Outline each blood parasite and name the species.
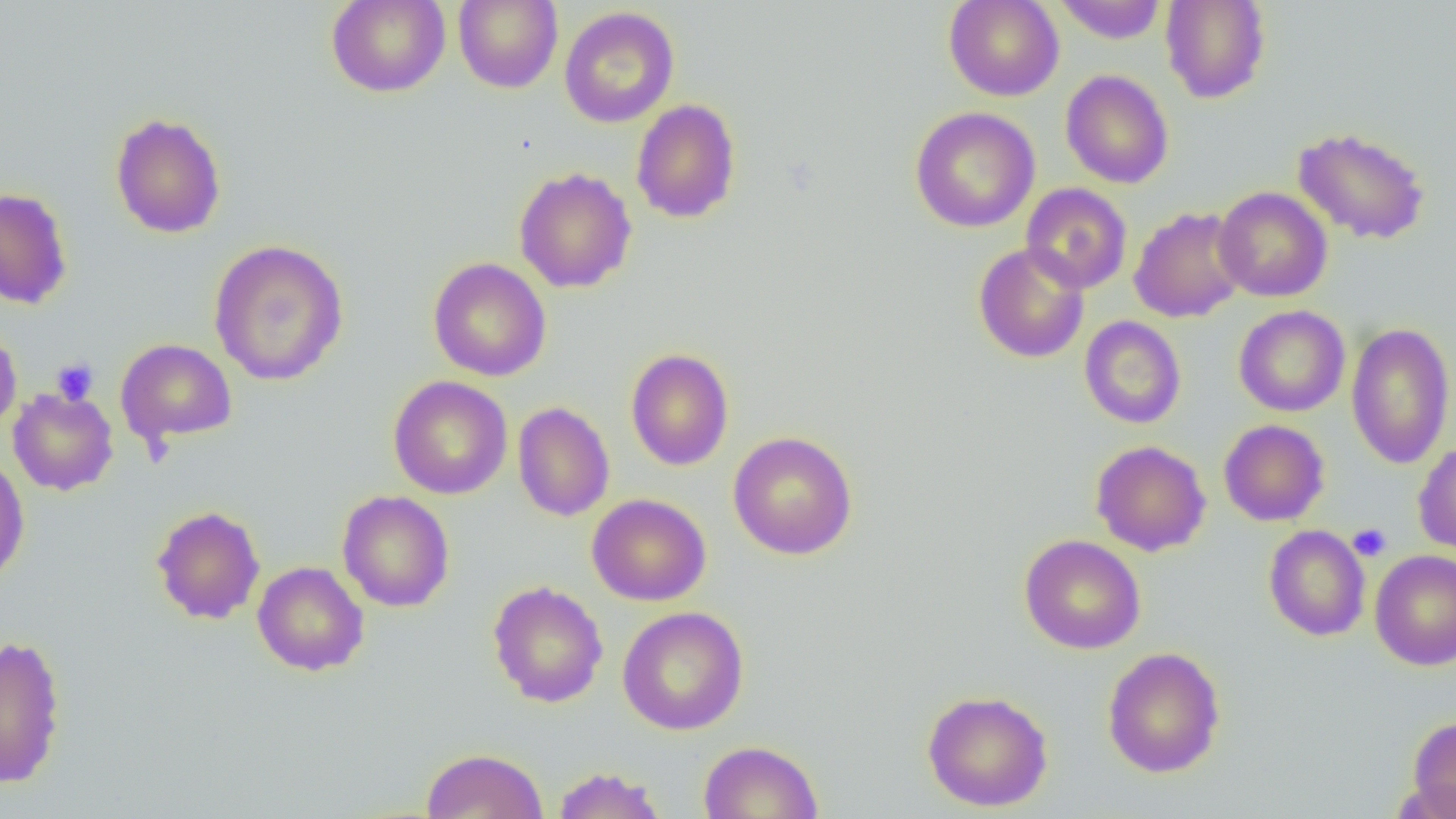
No blood parasites seen.

Approximate bounding boxes as named x1/y1/x2/y2 corners in pixels. Uninfected red blood cell locations: (x1=325, y1=0, x2=451, y2=98), (x1=453, y1=0, x2=563, y2=93), (x1=943, y1=0, x2=1064, y2=101), (x1=1053, y1=0, x2=1166, y2=44), (x1=1160, y1=0, x2=1272, y2=104), (x1=559, y1=6, x2=679, y2=128), (x1=1061, y1=69, x2=1174, y2=189), (x1=630, y1=99, x2=741, y2=224), (x1=910, y1=106, x2=1040, y2=232), (x1=110, y1=112, x2=226, y2=239), (x1=1292, y1=126, x2=1431, y2=245), (x1=513, y1=167, x2=637, y2=293), (x1=1021, y1=183, x2=1132, y2=294), (x1=1214, y1=186, x2=1333, y2=302), (x1=0, y1=187, x2=73, y2=309), (x1=1129, y1=206, x2=1248, y2=323), (x1=208, y1=238, x2=349, y2=386), (x1=973, y1=243, x2=1090, y2=364), (x1=428, y1=257, x2=552, y2=382), (x1=1233, y1=305, x2=1350, y2=417), (x1=1079, y1=316, x2=1186, y2=429), (x1=1345, y1=321, x2=1455, y2=469), (x1=0, y1=323, x2=22, y2=437), (x1=116, y1=338, x2=237, y2=447), (x1=625, y1=348, x2=734, y2=471), (x1=388, y1=376, x2=513, y2=499), (x1=8, y1=388, x2=118, y2=495), (x1=512, y1=402, x2=615, y2=521), (x1=1218, y1=419, x2=1330, y2=527), (x1=728, y1=430, x2=858, y2=560), (x1=1091, y1=440, x2=1211, y2=557), (x1=1413, y1=441, x2=1456, y2=557), (x1=0, y1=453, x2=30, y2=585), (x1=338, y1=490, x2=455, y2=612), (x1=587, y1=493, x2=712, y2=607), (x1=151, y1=505, x2=265, y2=625), (x1=1264, y1=525, x2=1371, y2=641), (x1=1019, y1=534, x2=1146, y2=654), (x1=1370, y1=550, x2=1456, y2=671), (x1=252, y1=561, x2=369, y2=676), (x1=487, y1=580, x2=608, y2=708), (x1=617, y1=606, x2=749, y2=734), (x1=0, y1=634, x2=67, y2=789), (x1=1102, y1=647, x2=1226, y2=778), (x1=922, y1=689, x2=1053, y2=812), (x1=1407, y1=715, x2=1456, y2=818), (x1=697, y1=740, x2=823, y2=819), (x1=420, y1=747, x2=548, y2=819), (x1=550, y1=766, x2=669, y2=819). Platelet locations: (x1=51, y1=358, x2=99, y2=405), (x1=1347, y1=523, x2=1392, y2=560). Slide-level diagnosis: no evidence of blood parasites. 1000x magnification. Thin blood film. Image is 1456×819 pixels. One field of a larger specimen. Optical microscopy.